Assess this cell for malaria.
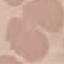

Uninfected.

Acquired by smartphone through the microscope eyepiece. Giemsa stain. Thin smear of blood. Automatically extracted cell patch, resized to 64 × 64 pixels.